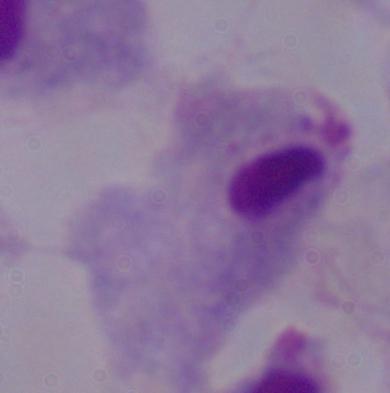

identification = trichomonad
magnification = 1000x
modality = micrograph